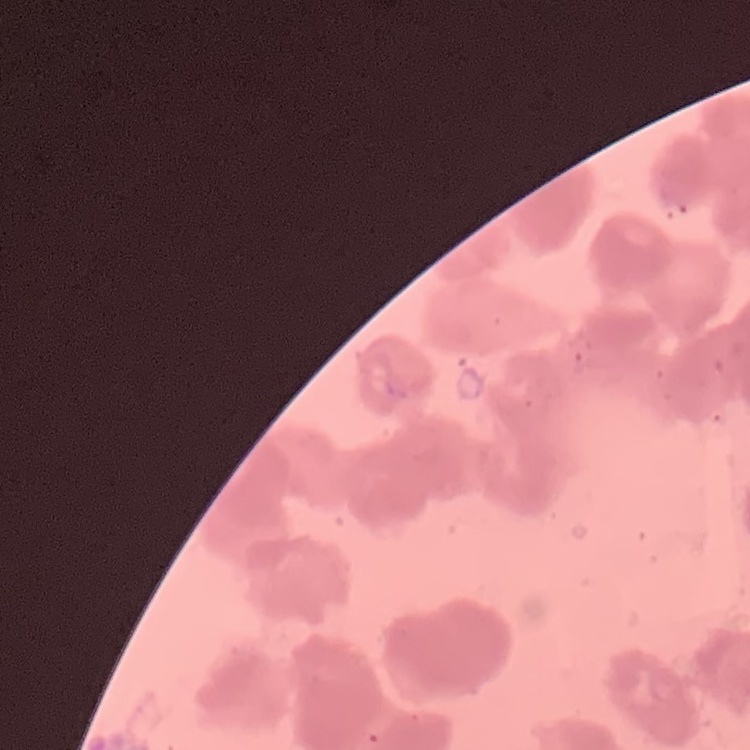

Summary:
  - Erythrocyte morphology: rouleaux formation
  - Image type: square crop of a larger photomicrograph
  - Stain: Field's or Giemsa
  - Preparation: thin blood film